Identify the blood parasite species.
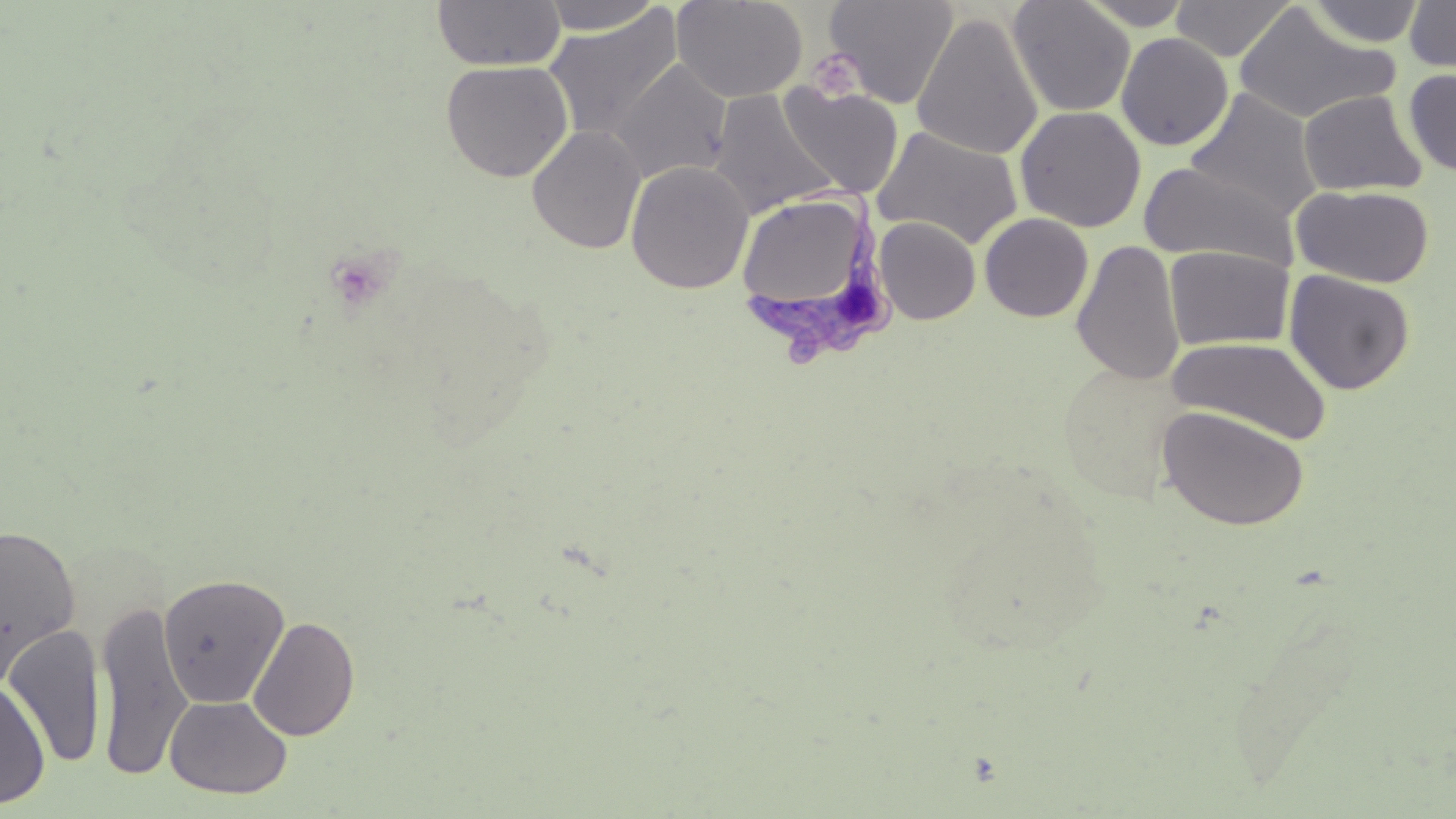

Trypanosoma brucei.

Approximate bounding boxes as named x1/y1/x2/y2 corners in pixels. Platelet locations: (x1=807, y1=48, x2=865, y2=101). Uninfected red blood cell locations: (x1=433, y1=0, x2=565, y2=71), (x1=538, y1=0, x2=664, y2=35), (x1=671, y1=0, x2=808, y2=104), (x1=824, y1=0, x2=958, y2=109), (x1=1008, y1=0, x2=1136, y2=117), (x1=1077, y1=0, x2=1195, y2=29), (x1=1170, y1=0, x2=1297, y2=61), (x1=1404, y1=0, x2=1456, y2=75), (x1=1307, y1=1, x2=1424, y2=47), (x1=1234, y1=4, x2=1399, y2=124), (x1=543, y1=7, x2=683, y2=143), (x1=911, y1=11, x2=1043, y2=160), (x1=1116, y1=32, x2=1233, y2=151), (x1=440, y1=59, x2=574, y2=182), (x1=610, y1=59, x2=733, y2=184), (x1=1403, y1=68, x2=1456, y2=176), (x1=780, y1=83, x2=904, y2=198), (x1=710, y1=89, x2=841, y2=217), (x1=1185, y1=89, x2=1321, y2=222), (x1=1298, y1=89, x2=1427, y2=196), (x1=1015, y1=105, x2=1146, y2=232), (x1=527, y1=125, x2=646, y2=254), (x1=872, y1=125, x2=1024, y2=249), (x1=625, y1=159, x2=753, y2=294), (x1=1139, y1=160, x2=1300, y2=269), (x1=1291, y1=184, x2=1435, y2=288), (x1=979, y1=213, x2=1094, y2=322), (x1=874, y1=217, x2=980, y2=325), (x1=1071, y1=239, x2=1185, y2=386), (x1=1164, y1=246, x2=1294, y2=351), (x1=1283, y1=269, x2=1415, y2=395), (x1=1167, y1=335, x2=1333, y2=445), (x1=1157, y1=405, x2=1310, y2=531), (x1=0, y1=523, x2=81, y2=683), (x1=158, y1=573, x2=290, y2=709), (x1=92, y1=600, x2=193, y2=782), (x1=247, y1=616, x2=360, y2=740), (x1=4, y1=625, x2=107, y2=768), (x1=0, y1=680, x2=50, y2=809), (x1=165, y1=695, x2=292, y2=799). Trypanosoma brucei locations: (x1=734, y1=194, x2=895, y2=362). Single field of view. Image is 1456×819 pixels. Captured at 1000x magnification. Thin blood film. May-Grünwald-Giemsa stain. Optical microscopy.